Comment on the morphology of the erythrocytes.
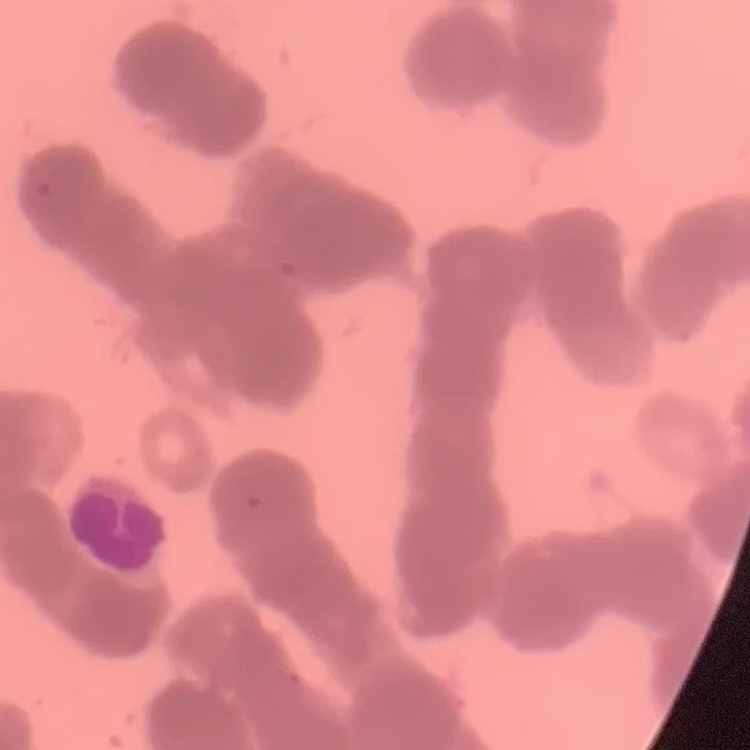

Rouleaux formation.

preparation = thin peripheral smear
image type = one tile cut from a larger photomicrograph
stain = Field's or Giemsa